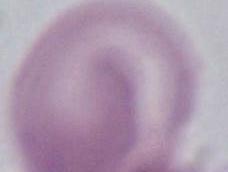
Micrograph. An erythrocyte is shown. Captured at 1000x magnification.